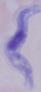 Micrograph. Captured at 1000x magnification. A trypanosome is seen.